Name the parasite shown.
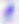
This is Toxoplasma gondii.

magnification = 400x
modality = micrograph